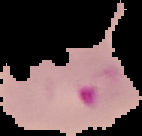
malaria_status: parasitized
image_size: 142×136 pixels
image_type: cell region segmented out of the field of view; surrounding area masked to black
preparation: thin blood film